Assess the morphology of the erythrocytes.
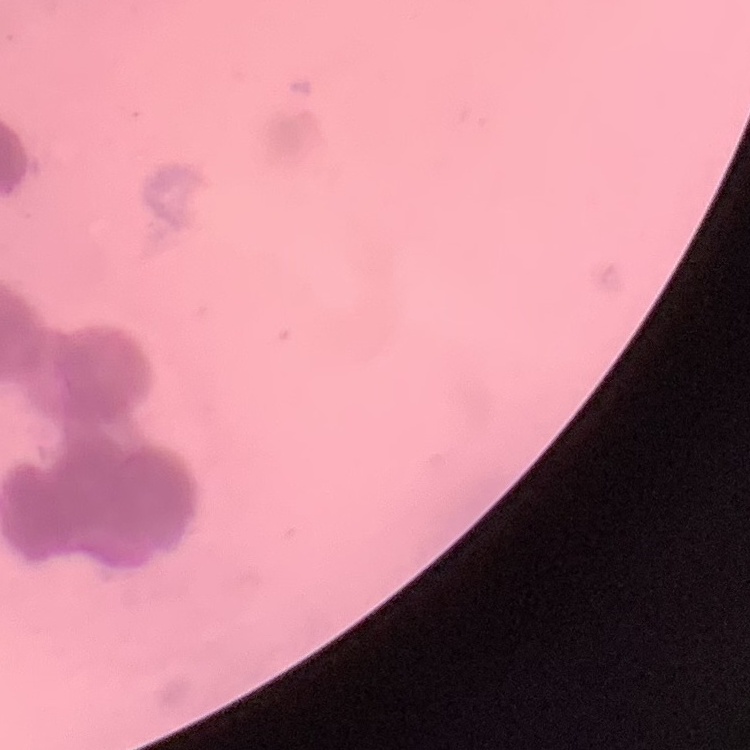
They show rouleaux formation.

Square crop of a larger photomicrograph. Stained with either Field's or Giemsa. Thin blood film.